Point out each Plasmodium parasite.
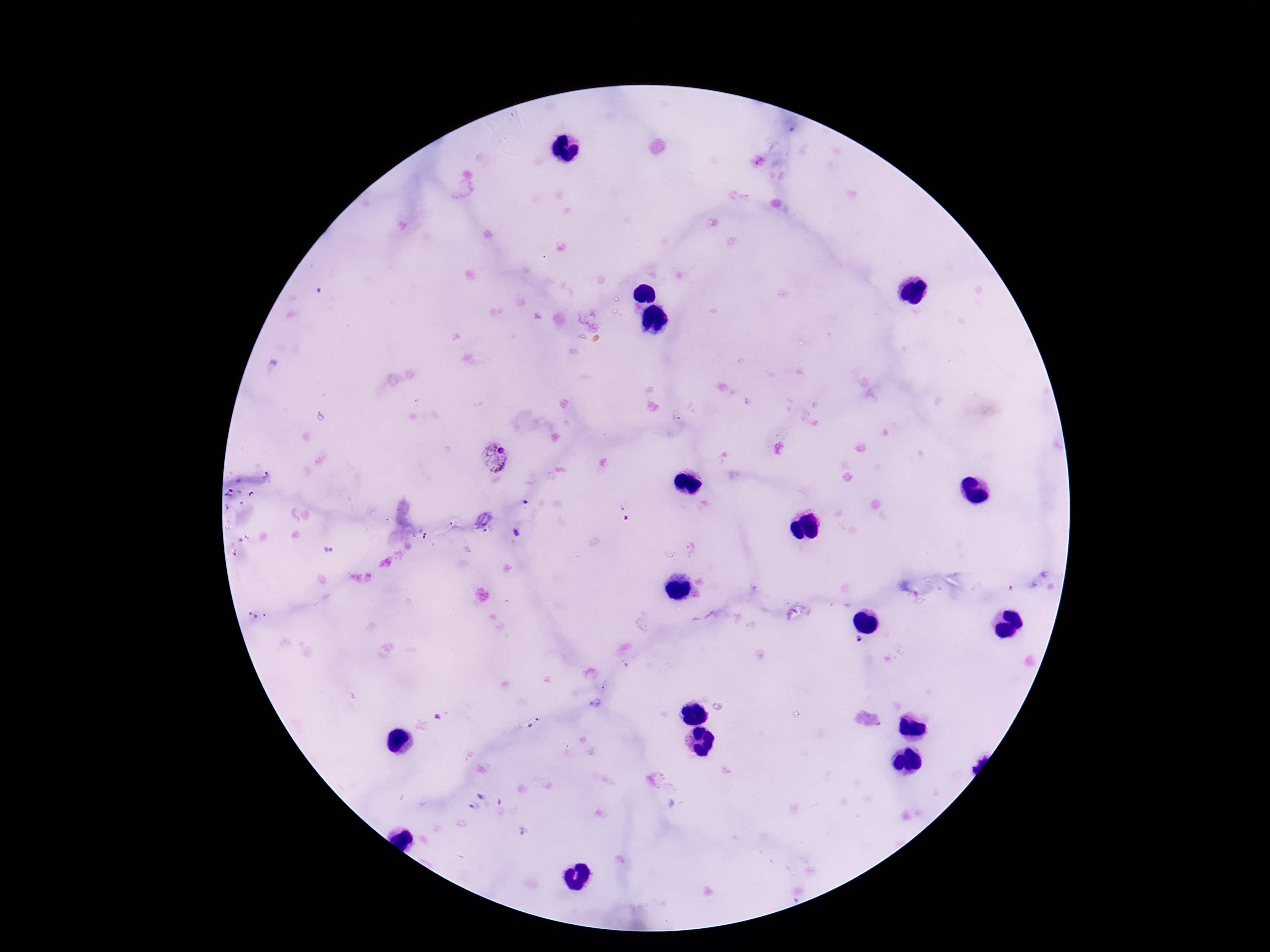

Approximate object centers, in pixels from the top-left corner.
Plasmodium parasites: (x=494, y=458).

Summary:
  - Field of view: one from this slide
  - Patient malaria status: positive
  - Capture: smartphone camera through the microscope eyepiece
  - Magnification: 100x
  - Preparation: thick peripheral-blood smear
  - Image size: 1270×952 pixels
  - Stain: Giemsa